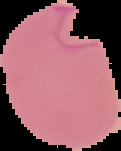 Image is 121×151 pixels. The area outside the segmented cell region is set to black. From a thin blood smear. Malaria status: parasitized.